Assess this cell for malaria.
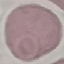

Uninfected.

Summary:
  - Stain: Giemsa
  - Capture: smartphone through the microscope eyepiece
  - Preparation: thin smear
  - Image type: cell patch, automatically extracted from a larger field of view and resized to 64 × 64 pixels